Name the parasite shown.
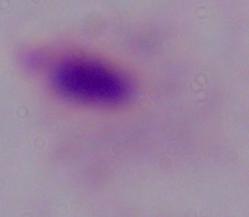
This is a trichomonad.

magnification: 1000x
modality: micrograph